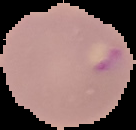

{
  "preparation": "thin blood film",
  "image_size": "136×130 pixels",
  "image_type": "segmented cell region on a black background",
  "result": "Plasmodium parasites detected"
}